State the blood parasite species.
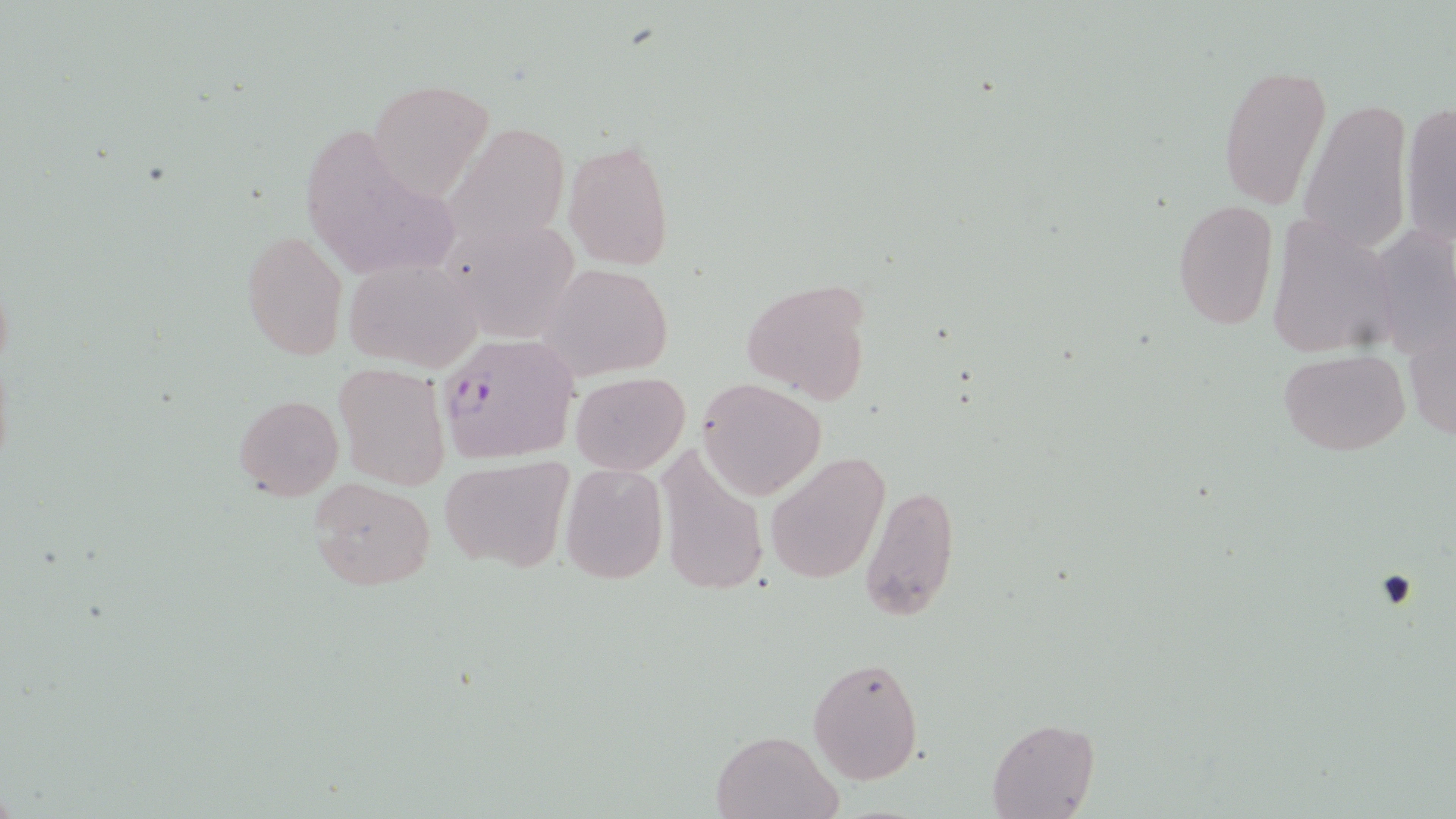

Plasmodium falciparum.

Summary:
  - Coordinate format: approximate bounding boxes as [x1, y1, x2, y2] in pixels
  - Plasmodium falciparum-infected red blood cell locations: [433, 332, 578, 464]
  - Uninfected red blood cell locations: [1218, 62, 1333, 207], [368, 79, 495, 197], [1298, 99, 1412, 260], [1400, 102, 1456, 249], [295, 116, 467, 287], [457, 124, 575, 245], [562, 138, 674, 270], [1172, 198, 1279, 332], [1268, 216, 1402, 359], [441, 222, 582, 343], [241, 226, 349, 362], [343, 256, 483, 371], [541, 263, 672, 379], [741, 276, 874, 403], [1403, 311, 1456, 450], [1277, 349, 1408, 456], [332, 364, 449, 490], [570, 372, 690, 473], [698, 379, 824, 500], [234, 395, 342, 500], [653, 440, 768, 596], [765, 453, 887, 583], [438, 456, 576, 573], [560, 463, 667, 584], [310, 479, 436, 589], [859, 482, 959, 621], [807, 654, 925, 785], [988, 719, 1099, 819], [710, 728, 843, 818]
  - Magnification: 1000x
  - Field of view: single
  - Modality: light microscopy
  - Stain: May-Grünwald-Giemsa
  - Image size: 1456×819 pixels
  - Preparation: thin blood smear